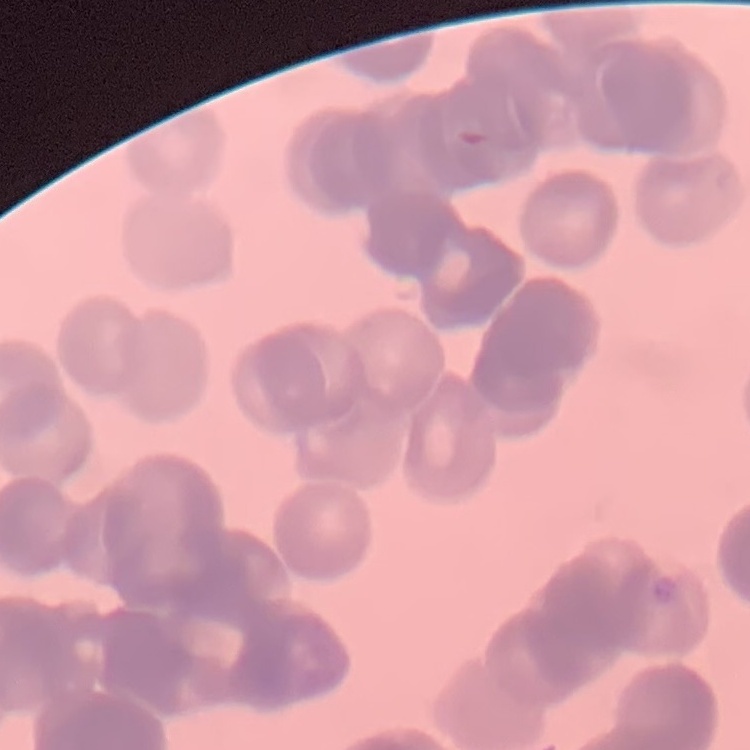

erythrocyte morphology = rouleaux formation
stain = Field's or Giemsa
image type = square crop of a larger photomicrograph
preparation = thin peripheral smear